Outline malaria parasites and classify them by life-cycle stage.
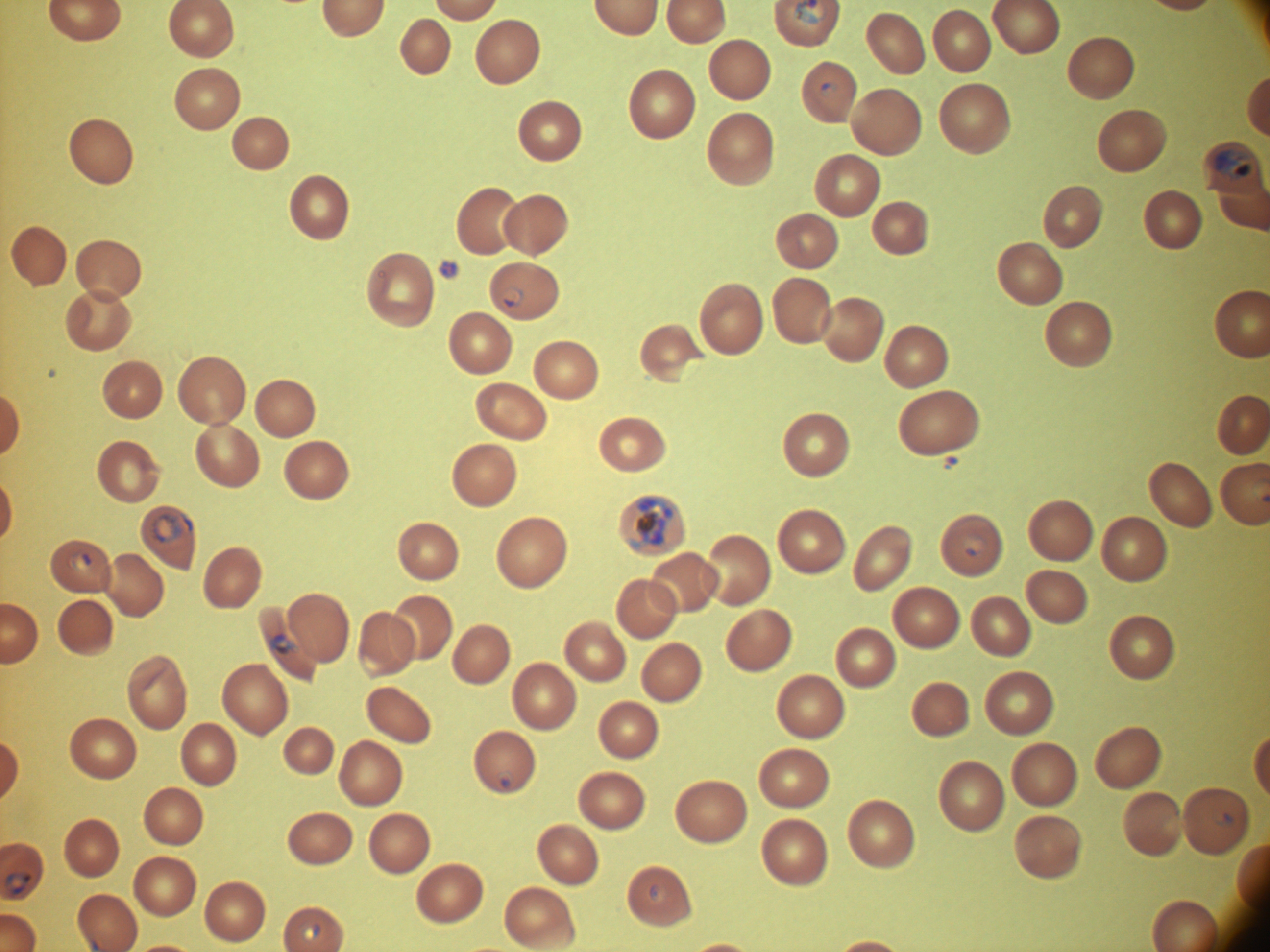

Approximate bounding boxes as [x1, y1, x2, y2] in pixels, from the source annotation, which is not necessarily exhaustive.
Ring forms: [822, 82, 837, 97], [503, 285, 524, 307], [151, 513, 183, 543], [962, 533, 987, 557], [71, 550, 92, 571], [496, 770, 514, 788], [1212, 811, 1236, 827], [3, 871, 32, 894], [649, 883, 667, 903], [298, 918, 321, 943].
Trophozoites: [269, 633, 299, 655].
Schizonts: [1215, 148, 1252, 181], [630, 495, 674, 549].

life-cycle stages among the annotated parasites = ring form, trophozoite, schizont
species = Plasmodium falciparum
field of view = single
magnification = 100x
microscope = Leica DM2000 with built-in camera
preparation = thin blood film
image size = 1270×952 pixels
stain = Giemsa